Locate every Babesia divergens-infected red blood cell.
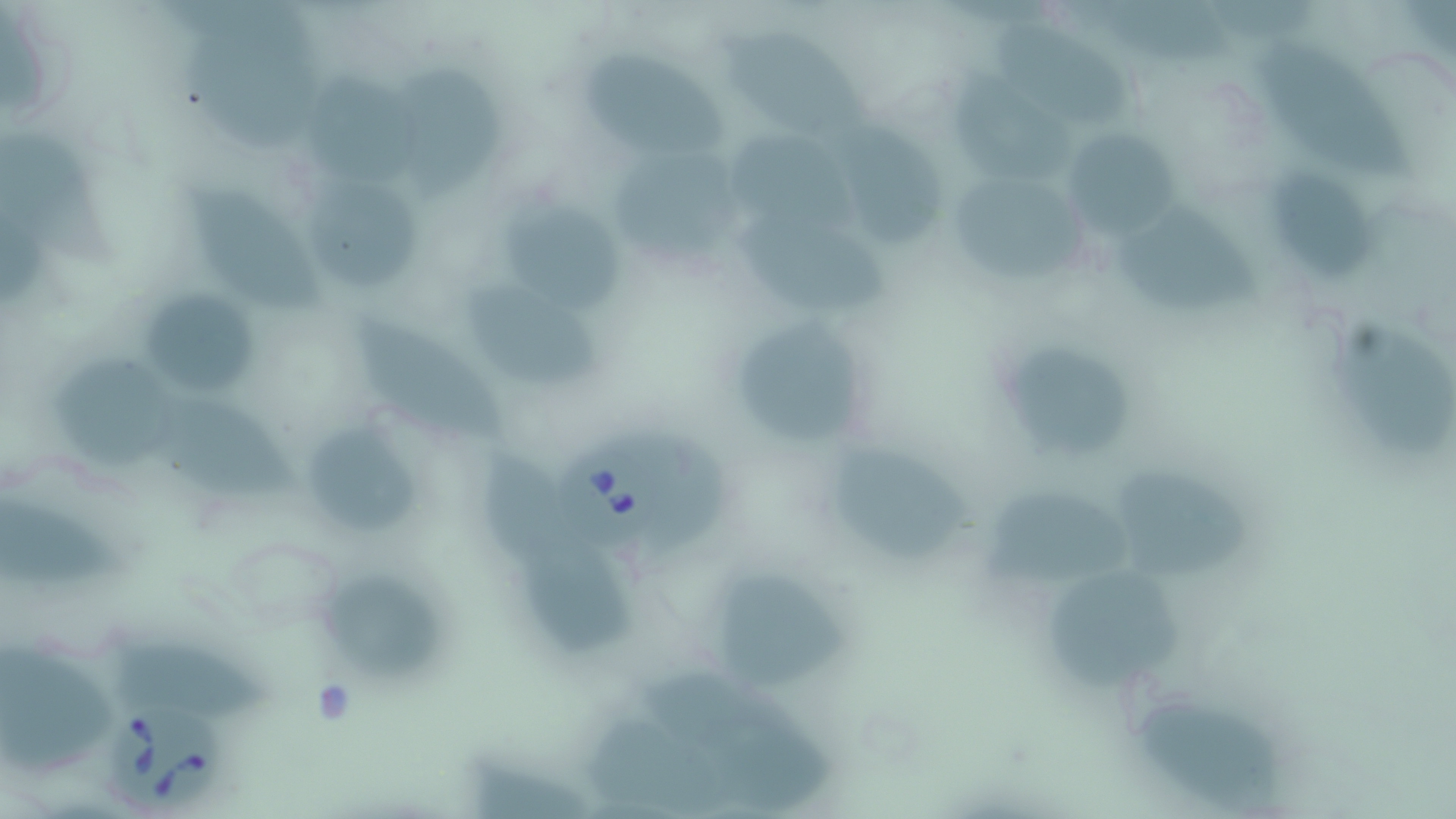
Approximate bounding boxes as [x1, y1, x2, y2] in pixels.
Babesia divergens-infected red blood cells: [548, 441, 671, 550], [109, 694, 226, 813].

Uninfected red blood cell locations: [1068, 0, 1235, 70], [990, 22, 1134, 132], [717, 27, 875, 143], [190, 34, 323, 153], [1259, 42, 1415, 184], [585, 51, 728, 156], [394, 66, 504, 199], [948, 72, 1073, 179], [307, 77, 418, 182], [834, 120, 944, 246], [1060, 126, 1179, 240], [728, 136, 856, 230], [610, 153, 741, 261], [944, 168, 1090, 287], [1271, 169, 1374, 286], [311, 180, 421, 294], [189, 185, 324, 313], [502, 202, 624, 317], [1112, 205, 1262, 316], [740, 213, 893, 310], [466, 285, 603, 388], [146, 296, 258, 398], [349, 313, 511, 444], [1342, 318, 1453, 465], [737, 320, 861, 442], [990, 336, 1144, 468], [49, 351, 180, 464], [160, 399, 300, 499], [306, 425, 419, 534], [484, 445, 575, 562], [839, 451, 971, 562], [1116, 476, 1255, 579], [981, 493, 1127, 588], [0, 499, 124, 585], [522, 545, 639, 656], [1049, 572, 1183, 692], [321, 576, 445, 682], [716, 576, 847, 687], [111, 639, 276, 727], [1, 645, 110, 774], [1141, 703, 1286, 813], [590, 715, 726, 813], [468, 753, 595, 819]. Slide-level diagnosis: Babesia divergens. May-Grünwald-Giemsa stain. Light microscopy. Single field of view. Captured at 1000x magnification. Image is 1456×819 pixels. Thin blood smear.